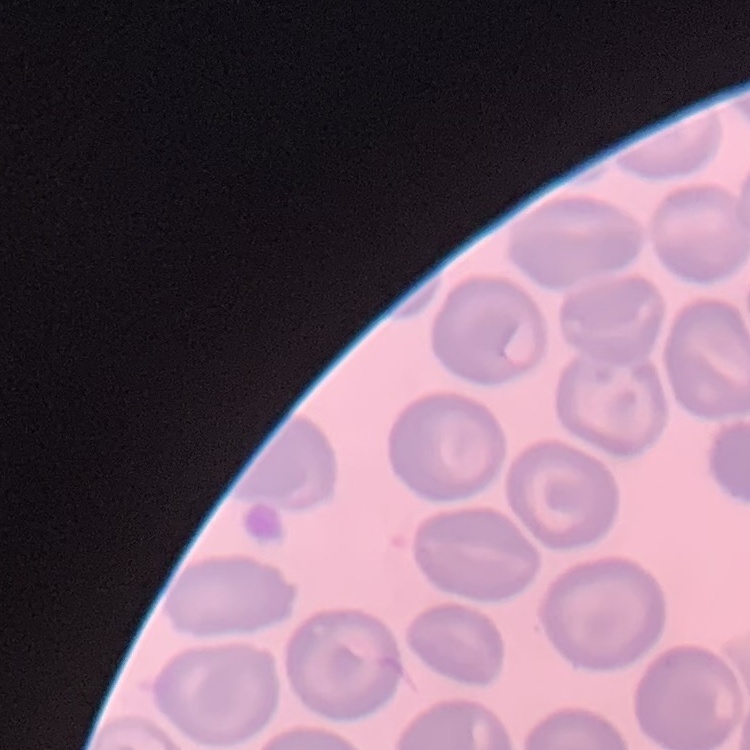

Summary:
  - Erythrocyte morphology: no rouleaux formation
  - Stain: Field's or Giemsa
  - Image type: one tile cut from a larger photomicrograph
  - Preparation: thin blood film